Locate every leukocyte (white blood cell).
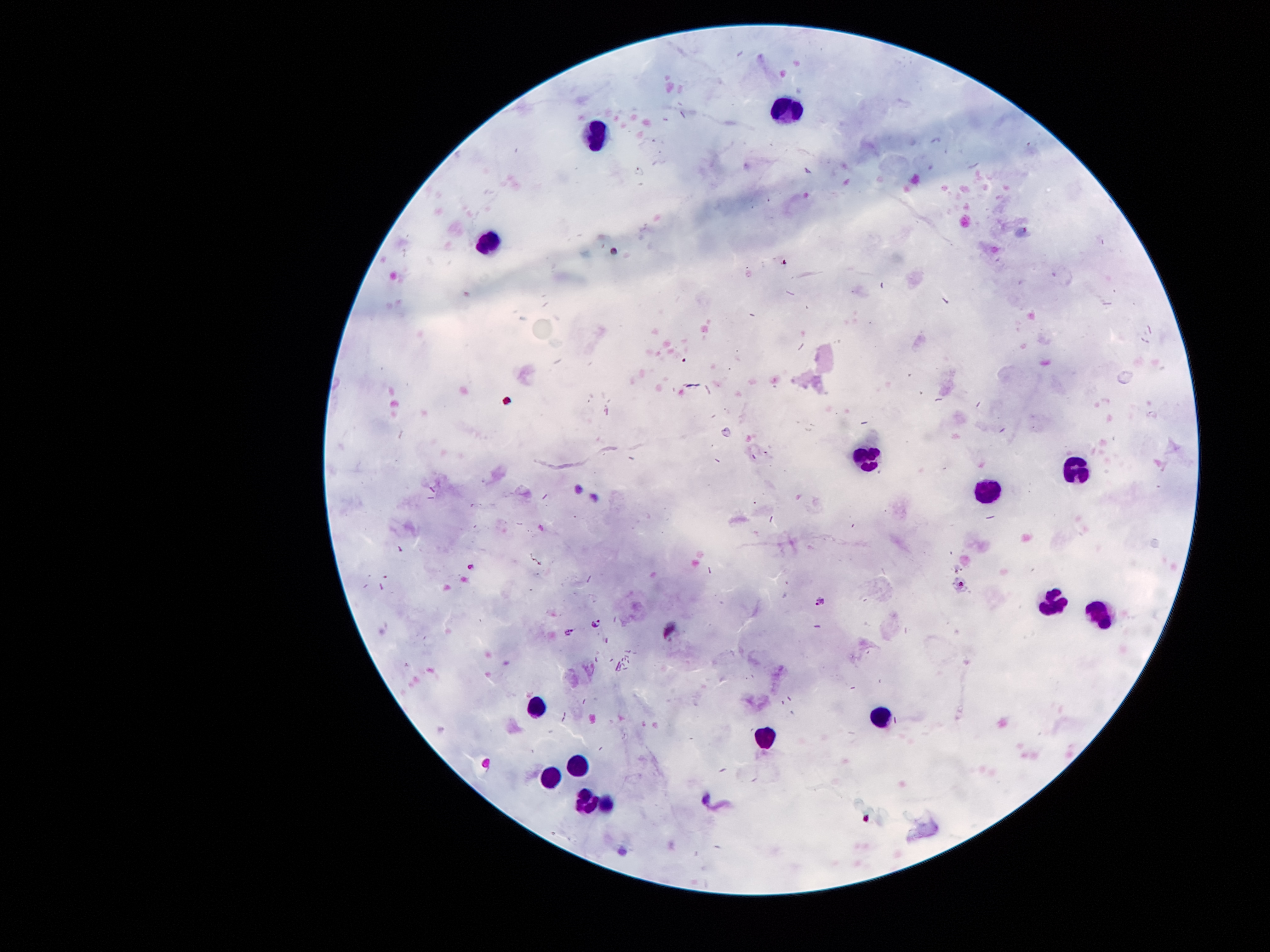
Approximate centers as [x, y] in pixels.
Leukocytes: [785, 108], [588, 135], [481, 240], [863, 458], [1076, 469], [985, 495], [1050, 603], [1099, 616], [536, 709], [882, 716], [763, 734], [578, 766], [549, 774], [582, 799].

stain: Giemsa
image_size: 1270×952 pixels
capture: smartphone camera through the microscope eyepiece
field_of_view: one from this slide
magnification: 100x
patient_malaria_status: infected with Plasmodium falciparum
preparation: thick peripheral-blood smear
malaria_parasite_locations: 'approximate centers as [x, y] in pixels: [472, 563], [821, 600], [596, 624], [571, 633]'